Classify this cell by malaria status.
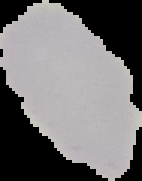
It is uninfected.

image_type: segmented cell region with the area outside set to black
preparation: thin blood film
image_size: 142×181 pixels